Identify the blood parasite species.
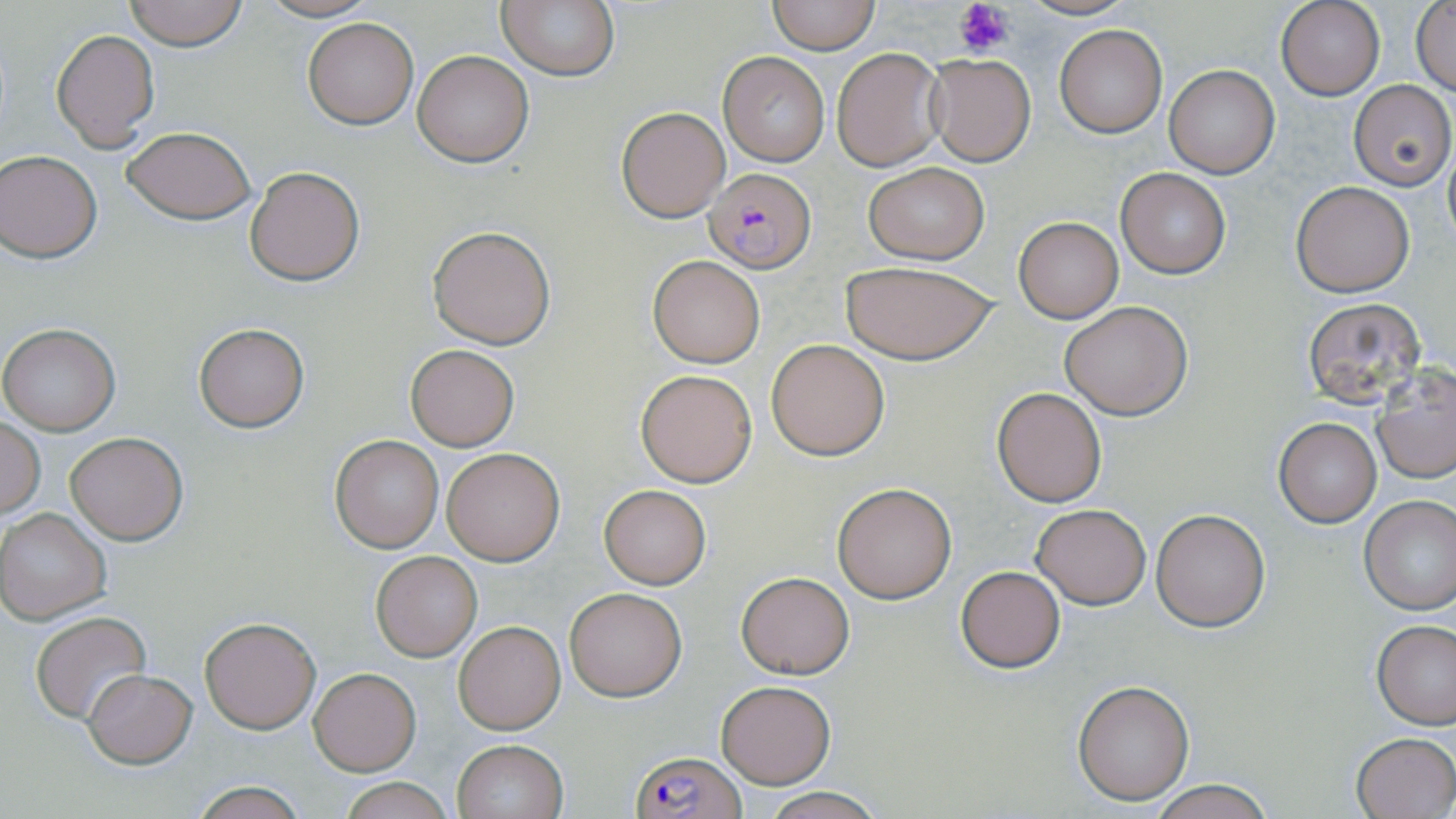

Plasmodium falciparum.

Summary:
  - Coordinate format: approximate bounding boxes as named x1/y1/x2/y2 corners in pixels
  - Plasmodium falciparum-infected red blood cell locations: (x1=703, y1=167, x2=817, y2=273), (x1=629, y1=748, x2=745, y2=818)
  - Platelet locations: (x1=955, y1=0, x2=1014, y2=58)
  - Uninfected red blood cell locations: (x1=121, y1=0, x2=250, y2=48), (x1=256, y1=0, x2=380, y2=23), (x1=768, y1=0, x2=879, y2=53), (x1=1015, y1=0, x2=1138, y2=21), (x1=497, y1=1, x2=620, y2=82), (x1=1276, y1=2, x2=1384, y2=101), (x1=1411, y1=2, x2=1456, y2=97), (x1=302, y1=18, x2=418, y2=129), (x1=1054, y1=25, x2=1168, y2=137), (x1=50, y1=28, x2=160, y2=152), (x1=830, y1=47, x2=946, y2=173), (x1=413, y1=50, x2=533, y2=166), (x1=716, y1=52, x2=831, y2=166), (x1=924, y1=54, x2=1036, y2=167), (x1=1165, y1=65, x2=1279, y2=179), (x1=1349, y1=80, x2=1455, y2=189), (x1=616, y1=106, x2=731, y2=222), (x1=122, y1=127, x2=257, y2=223), (x1=1442, y1=143, x2=1455, y2=249), (x1=0, y1=149, x2=101, y2=261), (x1=862, y1=162, x2=988, y2=264), (x1=245, y1=167, x2=364, y2=285), (x1=1115, y1=168, x2=1230, y2=278), (x1=1291, y1=181, x2=1416, y2=297), (x1=1013, y1=216, x2=1123, y2=322), (x1=428, y1=224, x2=556, y2=350), (x1=647, y1=254, x2=765, y2=368), (x1=840, y1=260, x2=999, y2=366), (x1=1302, y1=296, x2=1428, y2=407), (x1=1061, y1=301, x2=1193, y2=419), (x1=193, y1=321, x2=310, y2=433), (x1=0, y1=323, x2=120, y2=437), (x1=767, y1=339, x2=889, y2=460), (x1=406, y1=344, x2=520, y2=451), (x1=1373, y1=364, x2=1456, y2=485), (x1=636, y1=369, x2=757, y2=487), (x1=992, y1=386, x2=1108, y2=508), (x1=1273, y1=418, x2=1382, y2=527), (x1=2, y1=419, x2=44, y2=519), (x1=67, y1=432, x2=187, y2=545), (x1=330, y1=435, x2=443, y2=552), (x1=441, y1=448, x2=564, y2=566), (x1=831, y1=482, x2=957, y2=603), (x1=599, y1=485, x2=711, y2=589), (x1=1359, y1=495, x2=1456, y2=614), (x1=1031, y1=504, x2=1150, y2=609), (x1=1, y1=508, x2=113, y2=625), (x1=1150, y1=509, x2=1270, y2=630), (x1=371, y1=551, x2=481, y2=661), (x1=954, y1=564, x2=1067, y2=673), (x1=735, y1=570, x2=855, y2=678), (x1=563, y1=587, x2=687, y2=700), (x1=30, y1=611, x2=152, y2=723), (x1=200, y1=616, x2=321, y2=734), (x1=1372, y1=619, x2=1456, y2=729), (x1=453, y1=620, x2=565, y2=734), (x1=84, y1=667, x2=197, y2=767), (x1=310, y1=668, x2=420, y2=775), (x1=1072, y1=679, x2=1196, y2=805), (x1=717, y1=681, x2=835, y2=788), (x1=1350, y1=731, x2=1456, y2=817), (x1=451, y1=738, x2=568, y2=819), (x1=338, y1=776, x2=453, y2=819), (x1=1147, y1=779, x2=1275, y2=819), (x1=187, y1=781, x2=309, y2=818), (x1=757, y1=787, x2=889, y2=819)
  - Magnification: 1000x
  - Modality: optical microscopy
  - Stain: May-Grünwald-Giemsa
  - Field of view: single
  - Image size: 1456×819 pixels
  - Preparation: thin blood film